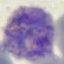 Malaria status: parasitized. Acquired by smartphone through the microscope eyepiece. Thin smear of blood. Giemsa stain. Automatically extracted cell patch, resized to 64 × 64 pixels.